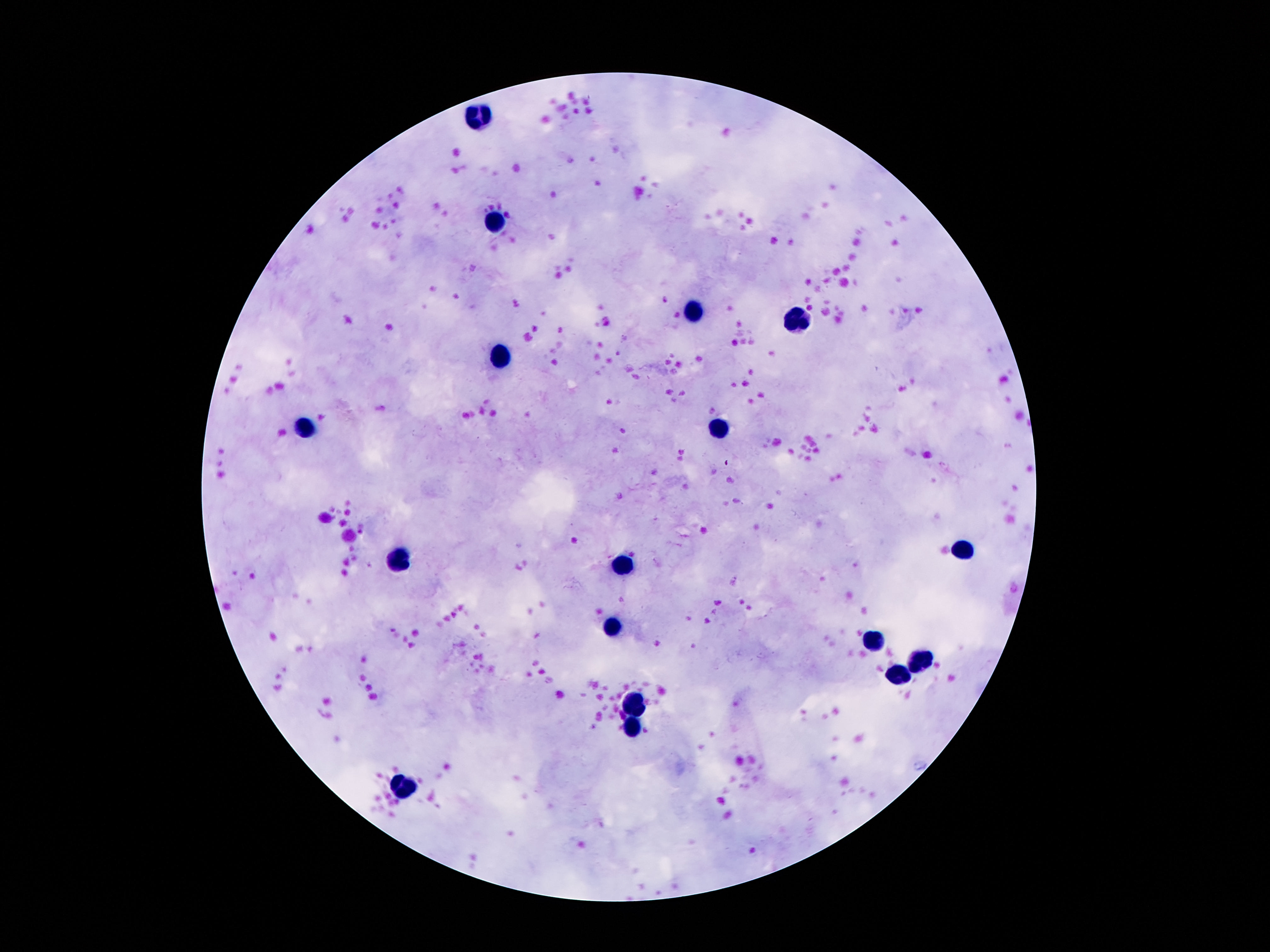

leukocyte locations = approximate object centers, in pixels from the top-left corner: (x=482, y=116), (x=497, y=223), (x=693, y=311), (x=798, y=321), (x=503, y=358), (x=305, y=429), (x=723, y=431), (x=964, y=549), (x=400, y=556), (x=624, y=564), (x=613, y=626), (x=873, y=639), (x=921, y=663), (x=895, y=677), (x=635, y=705), (x=632, y=730), (x=402, y=788)
patient malaria status = negative
capture = smartphone camera through the microscope eyepiece
field of view = one from this slide
image size = 1270×952 pixels
magnification = 100x
preparation = thick peripheral-blood smear
stain = Giemsa